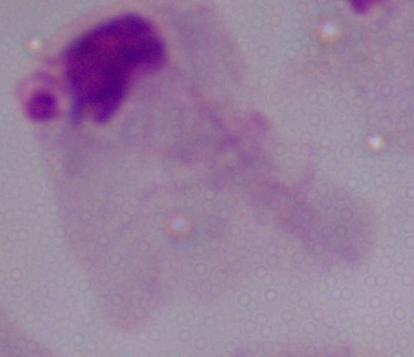

Summary:
  - Magnification: 1000x
  - Modality: micrograph
  - Identification: trichomonad